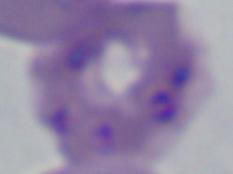 1000x magnification. Photomicrograph. A Babesia parasite is seen.